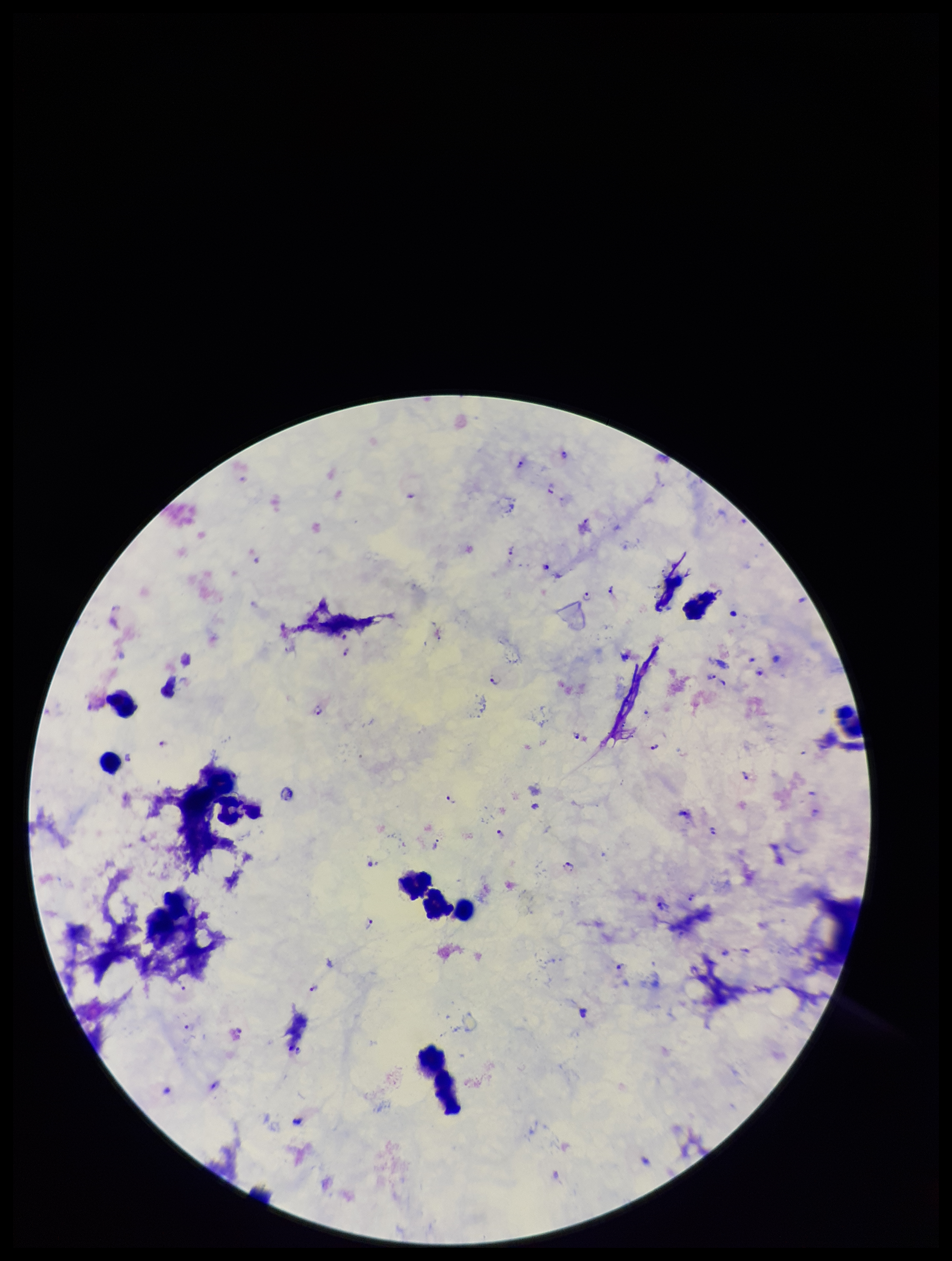

Summary:
  - Parasite count: 25
  - Plasmodium parasites: seen
  - Capture: smartphone photograph through the microscope eyepiece
  - Leukocyte count: 8
  - Field of view: one from this slide
  - Image size: 952×1261 pixels
  - Stain: Giemsa
  - Patient malaria status: positive
  - Species reported for this patient: Plasmodium falciparum
  - Preparation: thick smear